Give the position of every leukocyte visible.
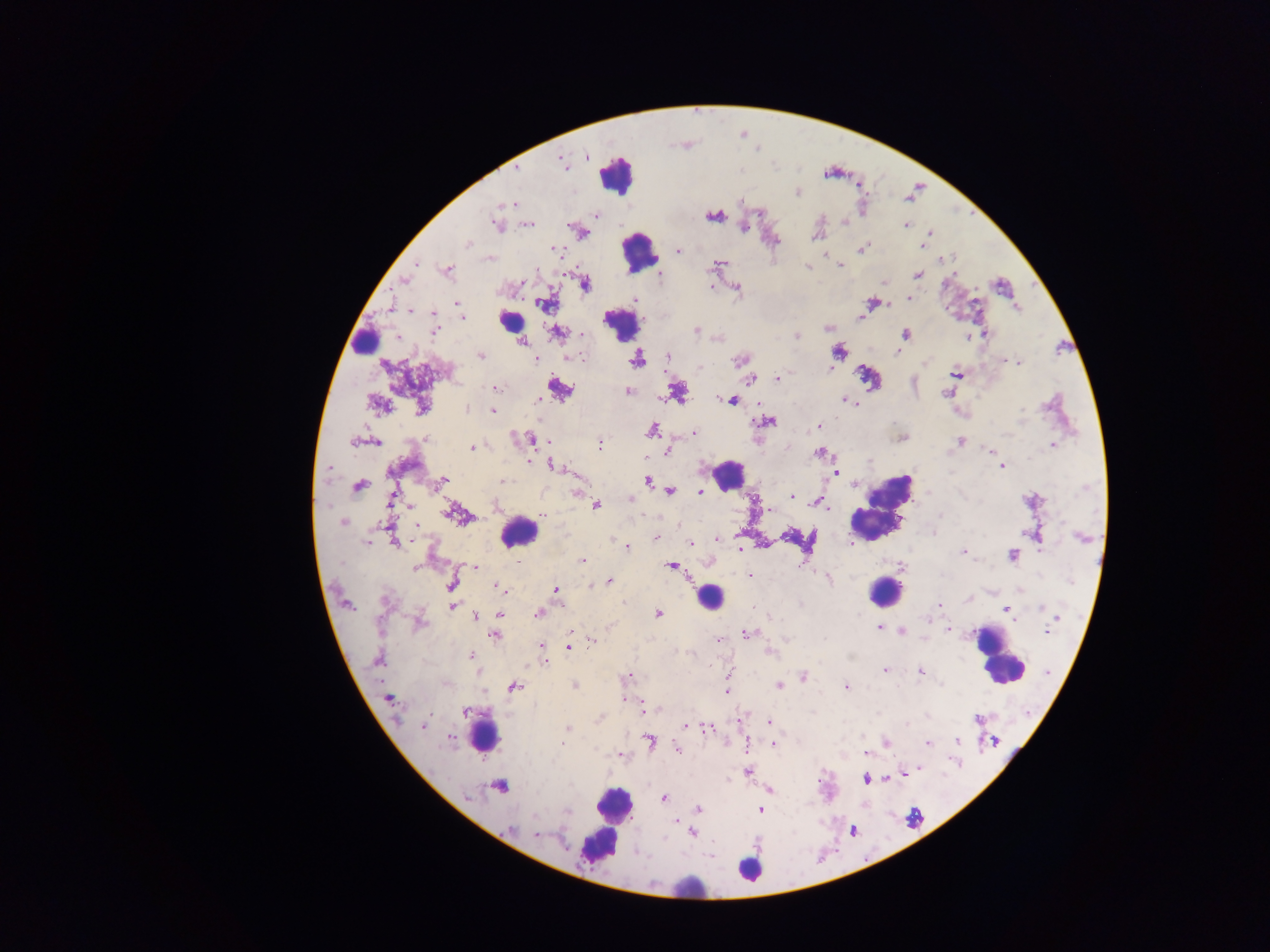

Approximate centers as (x, y) in pixels.
Leukocytes: (616, 174), (639, 253), (511, 321), (622, 326), (362, 334), (727, 474), (881, 508), (518, 532), (886, 591), (709, 598), (996, 657), (485, 734), (613, 805), (600, 842), (749, 870), (684, 885).

preparation = thick blood film
country = Ghana
image size = 1270×952 pixels
malaria parasite locations = approximate centers as (x, y) in pixels: (563, 163), (516, 168), (797, 192), (510, 203), (595, 215), (714, 215), (844, 222), (495, 224), (528, 225), (906, 225), (744, 227), (930, 233), (584, 234), (816, 236), (467, 244), (922, 246), (863, 248), (553, 249), (679, 251), (945, 259), (416, 263), (719, 264), (840, 265), (808, 267), (447, 271), (918, 275), (403, 279), (521, 283), (884, 283), (585, 284), (710, 286), (737, 288), (635, 299), (909, 299), (872, 303), (457, 304), (545, 305), (410, 311), (434, 316), (462, 318), (828, 328), (435, 331), (696, 331), (558, 333), (583, 335), (905, 335), (984, 335), (797, 336), (522, 343), (898, 351), (839, 352), (480, 356), (570, 356), (667, 356), (536, 358), (637, 359), (740, 360), (1019, 362), (925, 363), (700, 368), (830, 368), (956, 374), (777, 378), (751, 379), (496, 387), (559, 389), (628, 391), (677, 392), (946, 394), (732, 400), (537, 401), (847, 401), (852, 403), (378, 405), (422, 408), (467, 409), (493, 410), (766, 422), (819, 426), (651, 430), (694, 433), (530, 439), (902, 439), (960, 441), (352, 442), (377, 442), (600, 445), (1052, 445), (472, 448), (991, 451), (667, 452), (819, 452), (530, 462), (554, 466), (1002, 467), (329, 469), (836, 473), (647, 481), (442, 482), (505, 482), (358, 486), (577, 491), (670, 492), (702, 492), (791, 496), (390, 498), (630, 499), (495, 505), (822, 505), (596, 506), (827, 508), (769, 510), (455, 514), (542, 514), (940, 515), (343, 523), (417, 526), (655, 538), (717, 538), (613, 539), (395, 541), (690, 544), (627, 546), (963, 553), (1012, 555), (582, 561), (673, 566), (476, 567), (901, 567), (416, 569), (750, 575), (609, 581), (452, 584), (499, 588), (556, 590), (503, 591), (939, 604), (452, 606), (1041, 607), (1004, 609), (539, 613), (658, 613), (499, 614), (475, 616), (419, 622), (878, 627), (948, 630), (1047, 631), (902, 632), (747, 634), (494, 636), (720, 639), (592, 640), (542, 647), (569, 647), (769, 652), (472, 656), (377, 659), (545, 662), (885, 669), (921, 671), (729, 674), (628, 676), (803, 676), (941, 684), (574, 685), (779, 686), (514, 687), (846, 687), (726, 691), (388, 699), (625, 699), (644, 709), (464, 711), (599, 719), (978, 719), (769, 722), (907, 723), (424, 726), (685, 727), (567, 728), (709, 729), (449, 737), (650, 741), (957, 741), (995, 741), (562, 743), (886, 743), (773, 744), (928, 744), (678, 750), (866, 753), (619, 755), (918, 767), (748, 771), (866, 780), (500, 786), (769, 791), (468, 798), (664, 799), (698, 809), (760, 810), (567, 812), (535, 816), (675, 822), (511, 829), (692, 833), (535, 834)
field of view = single
capture = mobile-phone photograph through a microscope